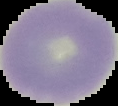
Summary:
  - Preparation: thin blood film
  - Image size: 118×106 pixels
  - Malaria status: uninfected
  - Image type: cell region segmented out of the field of view; surrounding area masked to black